Classify this cell by malaria status.
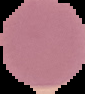
It is uninfected.

Segmented cell region on a black background. From a thin blood smear. Image is 85×94 pixels.